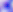

identification = Toxoplasma gondii
modality = photomicrograph
magnification = 400x